Point out each Plasmodium parasite and each leukocyte.
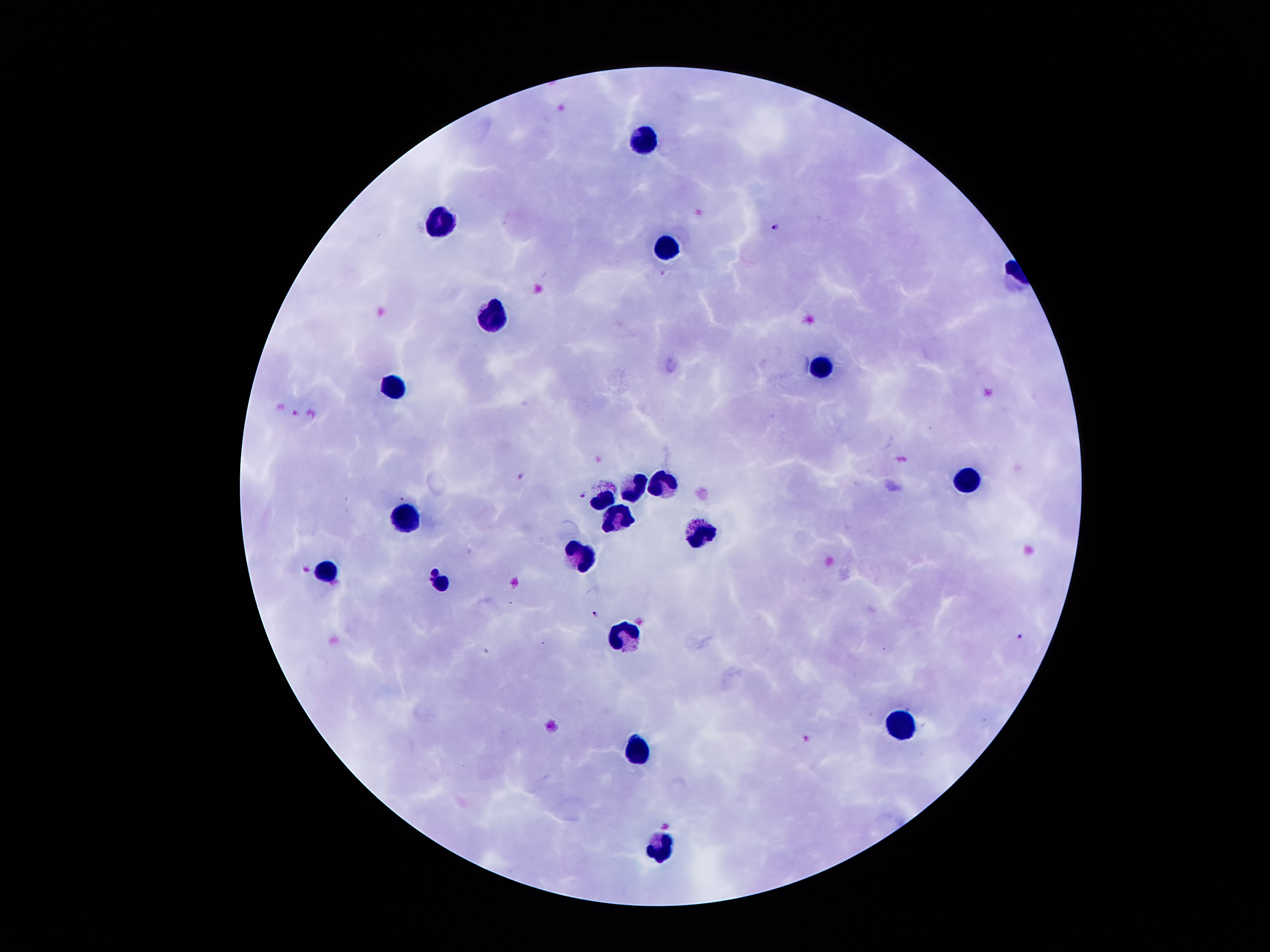

Approximate centers as (x, y) in pixels.
Plasmodium parasites: (776, 226), (294, 411), (520, 474), (583, 495), (594, 614), (1020, 635).
Leukocytes: (641, 142), (443, 224), (665, 247), (498, 320), (822, 369), (394, 385), (966, 478), (662, 485), (636, 486), (603, 500), (619, 516), (405, 519), (699, 536), (583, 555), (325, 569), (440, 583), (624, 636), (902, 723), (638, 751), (658, 844).

capture = smartphone camera through the microscope eyepiece
patient malaria status = positive for Plasmodium falciparum
image size = 1270×952 pixels
magnification = 100x
preparation = thick blood film
stain = Giemsa
field of view = one from this slide